Locate the red blood cells and classify each one as P. falciparum-infected, uninfected, or of indeterminate infection status.
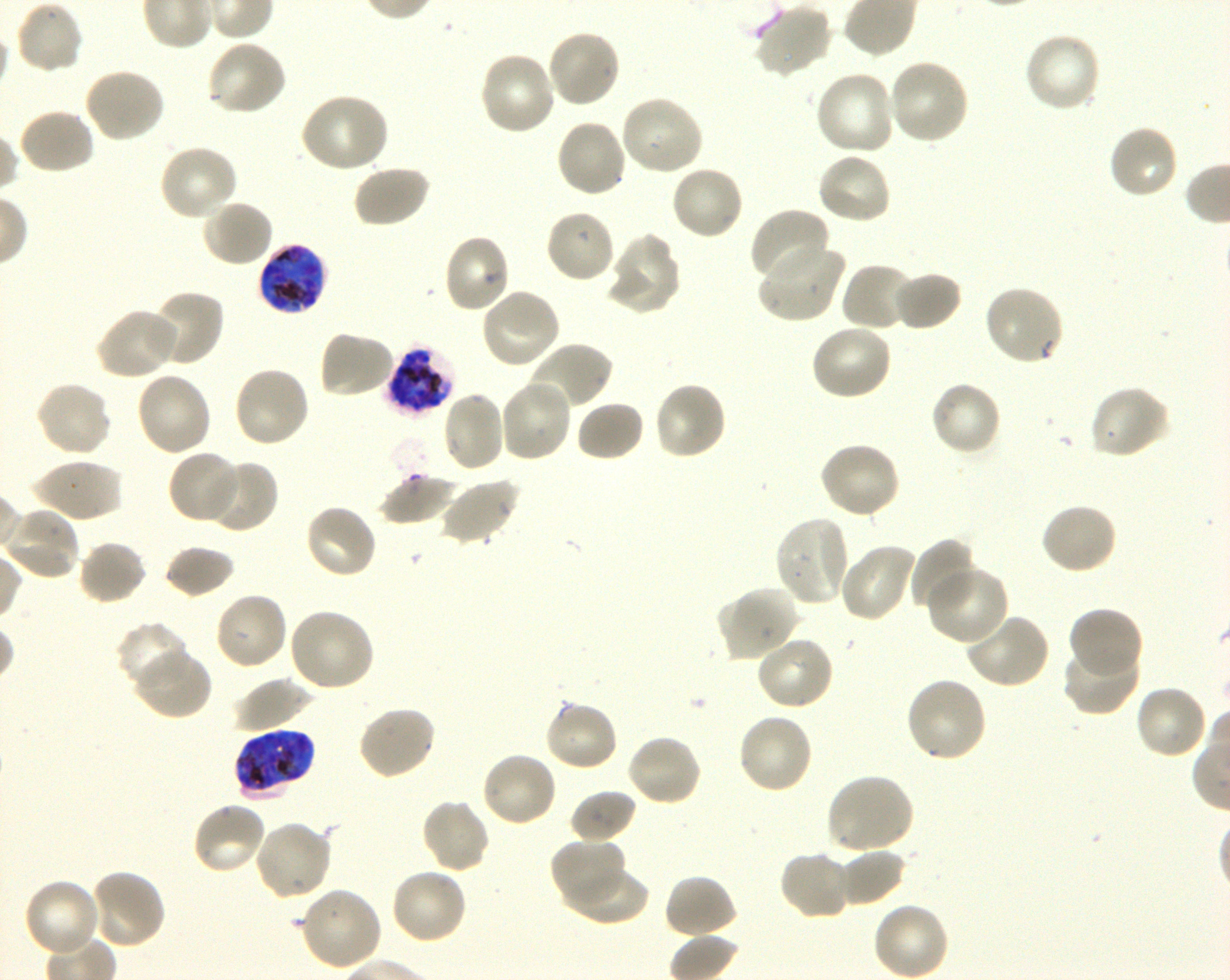
Approximate bounding boxes as {x1, y1, x2, y2} in pixels. Not every red blood cell is marked. A life-cycle stage — or a range of stages, where the recorded stages span more than one — follows each staged infected red blood cell.
Infected red blood cells: {256, 241, 329, 315} early trophozoite to late schizont; {385, 343, 456, 415} schizont; {235, 729, 313, 796} late trophozoite to late schizont.
Uninfected red blood cells: {13, 0, 84, 76}, {753, 2, 833, 78}, {546, 28, 622, 109}, {1022, 33, 1102, 114}, {206, 39, 288, 118}, {478, 51, 557, 137}, {888, 58, 970, 144}, {82, 67, 165, 143}, {814, 70, 897, 156}, {300, 92, 390, 174}, {618, 93, 704, 177}, {16, 108, 96, 176}, {555, 118, 628, 199}, {1107, 123, 1179, 200}, {158, 142, 239, 221}, {816, 152, 893, 227}, {352, 164, 431, 228}, {670, 164, 745, 240}, {201, 198, 274, 268}, {544, 208, 617, 285}, {748, 208, 830, 284}, {442, 233, 512, 314}, {608, 233, 681, 314}, {756, 240, 846, 325}, {839, 261, 918, 333}, {891, 270, 963, 332}, {983, 285, 1066, 366}, {479, 287, 562, 369}, {148, 290, 225, 367}, {94, 307, 180, 381}, {810, 322, 893, 401}, {318, 330, 396, 400}, {527, 341, 614, 413}, {232, 364, 311, 449}, {134, 370, 212, 458}, {498, 378, 573, 463}, {35, 380, 114, 458}, {930, 380, 1003, 456}, {653, 381, 728, 461}, {1089, 385, 1172, 460}, {441, 390, 506, 473}, {575, 399, 646, 462}, {817, 441, 901, 520}, {166, 450, 241, 524}, {33, 458, 124, 523}, {203, 459, 279, 533}, {379, 474, 457, 526}, {439, 477, 521, 546}, {1040, 502, 1119, 575}, {303, 503, 379, 580}, {4, 506, 81, 581}, {773, 515, 851, 607}, {910, 537, 979, 614}, {77, 540, 147, 607}, {838, 542, 918, 623}, {164, 545, 236, 600}, {926, 564, 1009, 646}, {716, 587, 797, 663}, {213, 591, 288, 672}, {1068, 606, 1144, 679}, {286, 607, 376, 693}, {962, 612, 1051, 690}, {116, 621, 190, 694}, {755, 634, 835, 710}, {1062, 641, 1141, 716}, {133, 648, 213, 720}, {233, 676, 314, 733}, {904, 676, 989, 763}, {1134, 684, 1209, 760}, {543, 699, 620, 773}, {357, 705, 438, 781}, {737, 712, 814, 795}, {625, 733, 703, 807}, {480, 750, 559, 828}, {824, 773, 914, 855}, {569, 790, 637, 845}, {421, 798, 491, 874}, {191, 800, 268, 876}, {252, 819, 333, 901}, {550, 837, 626, 909}, {837, 847, 907, 907}, {778, 850, 855, 921}, {389, 866, 468, 945}, {565, 866, 648, 927}, {87, 868, 167, 950}, {663, 874, 738, 941}, {22, 878, 102, 959}, {298, 886, 383, 972}, {873, 901, 950, 980}.
No red blood cells of indeterminate infection status observed.

Summary:
  - Preparation: thin blood smear
  - Donor blood group: O+
  - Stain: Giemsa
  - Image size: 1230×980 pixels
  - Field of view: one from this slide
  - Culture: P. falciparum strain 3D7, shaking, in vitro
  - Objective: 100x, oil immersion, numerical aperture 1.30